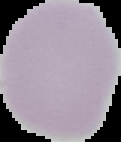 The area outside the segmented cell region is set to black. Image is 121×142 pixels. From a thin blood film. Result: negative for Plasmodium parasites.